Assess the morphology of the red blood cells.
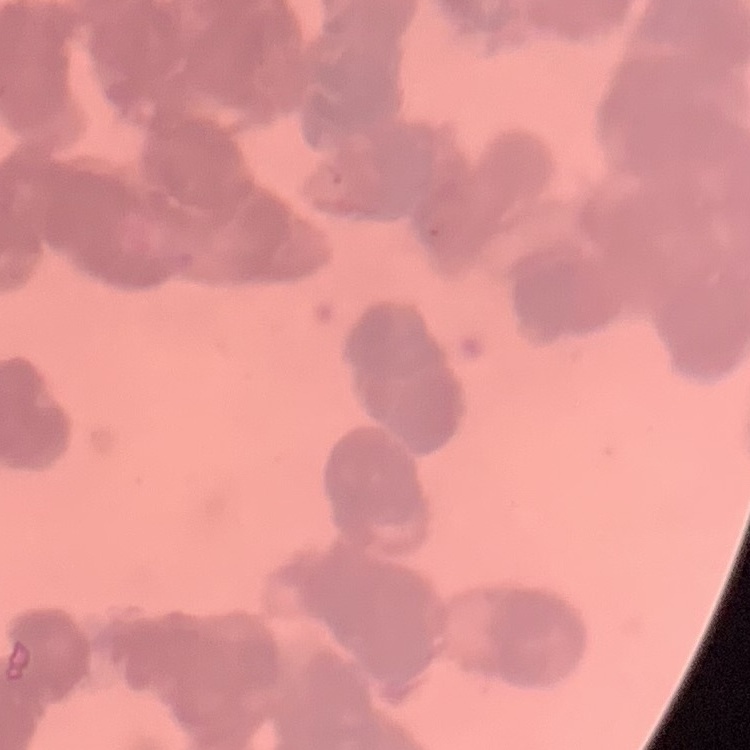
They show rouleaux formation.

Thin blood film. Square crop of a larger photomicrograph. Field's or Giemsa stain.